Report the malaria status of this cell.
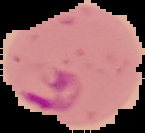

Parasitized.

Image is 145×133 pixels. From a thin blood smear. Cell region segmented out of the field of view; the surrounding area is masked to black.